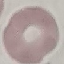

Result: negative for malaria parasites. Cell patch, automatically extracted from a larger field of view and resized to 64 × 64 pixels. Photographed with a smartphone camera at the microscope eyepiece. Giemsa stain. Thin blood film.